Identify the parasite.
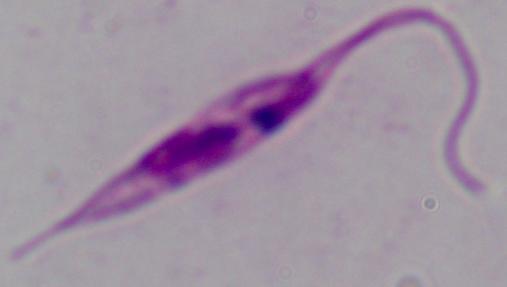
This is Leishmania.

Captured at 1000x magnification. Micrograph.